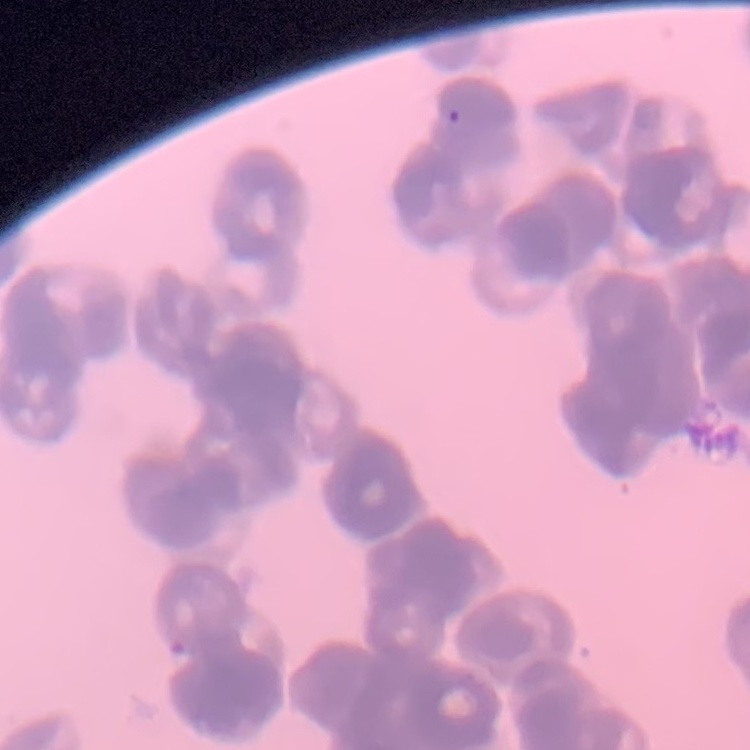
The erythrocytes exhibit rouleaux formation. Stained with either Field's or Giemsa. Thin blood smear. Square crop of a larger photomicrograph.